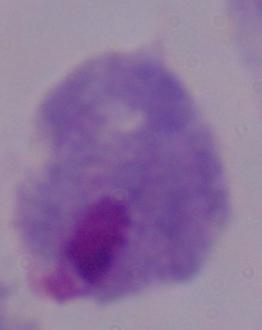

Captured at 1000x magnification. Photomicrograph. A trichomonad is seen.